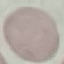 Result: no malaria parasites detected. Cell patch, automatically extracted from a larger field of view and resized to 64 × 64 pixels. Thin blood film. Photographed with a smartphone camera at the microscope eyepiece. Giemsa-stained preparation.